Point out each malaria parasite.
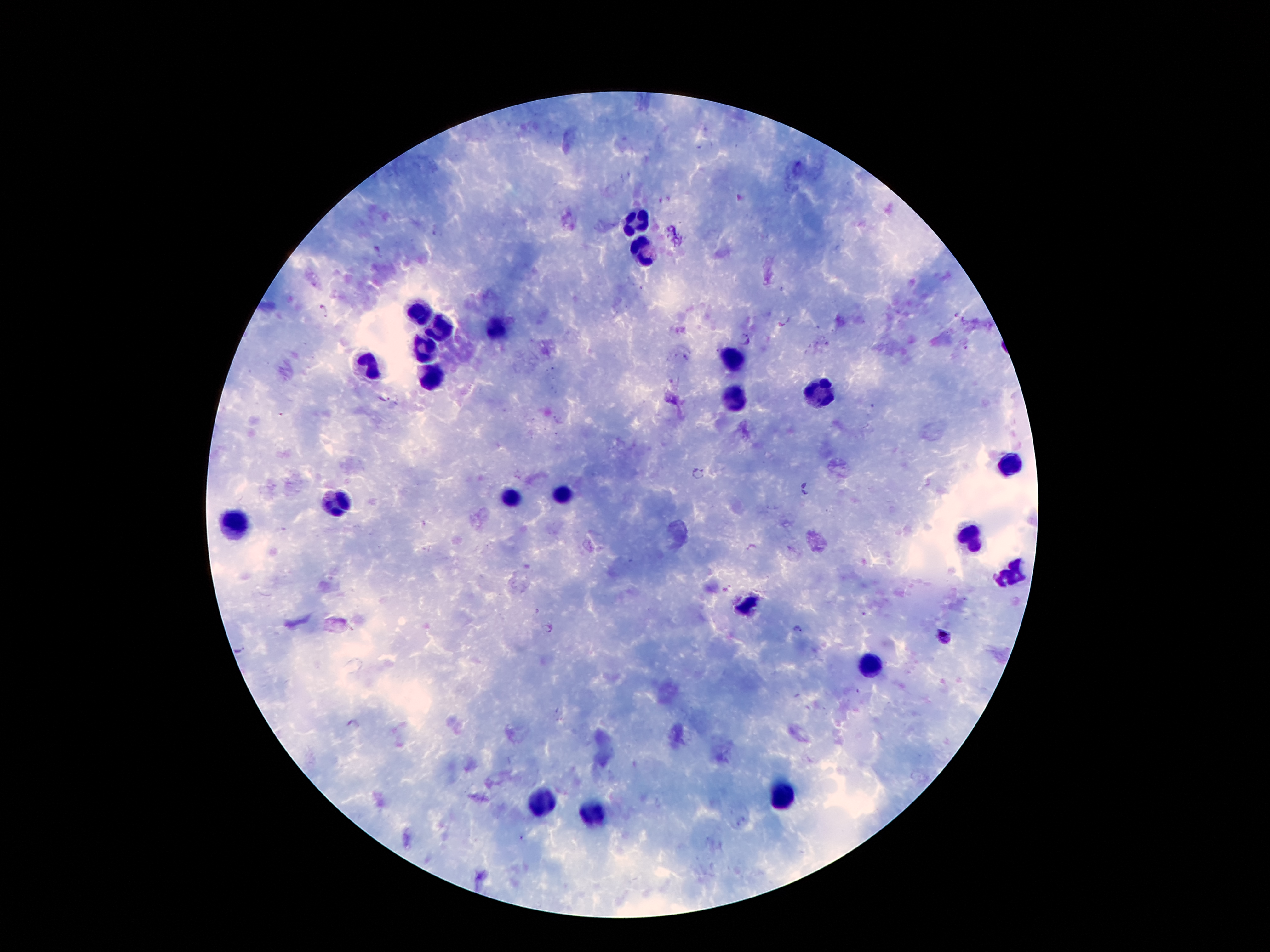

Approximate centers as (x, y) in pixels.
Malaria parasites: (323, 310), (785, 321), (745, 340), (383, 399), (697, 471), (808, 488), (547, 629), (797, 629), (944, 636), (355, 725).

Leukocyte locations: (638, 221), (644, 248), (420, 309), (441, 328), (497, 328), (426, 349), (730, 356), (365, 364), (434, 374), (821, 395), (733, 398), (1010, 463), (562, 498), (510, 499), (338, 501), (229, 522), (970, 536), (1010, 576), (746, 607), (871, 667), (786, 792), (535, 798), (593, 815). Smartphone photograph taken through the microscope eyepiece. Giemsa stain. Image is 1270×952 pixels. Single field of view. Patient malaria status: positive for Plasmodium falciparum. 100x magnification. Thick blood smear.